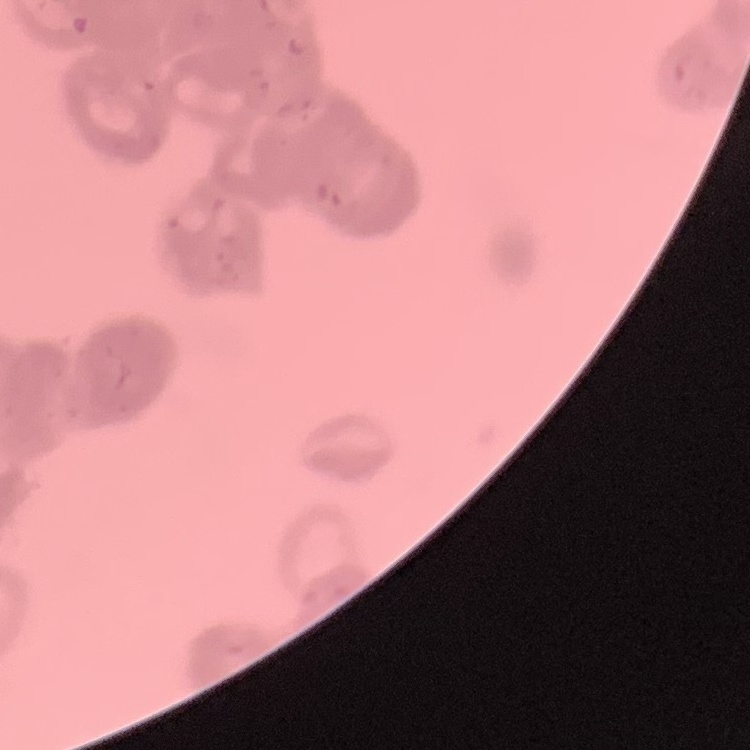
The red blood cells exhibit rouleaux formation. Square crop of a larger photomicrograph. Thin blood smear. Field's or Giemsa stain.